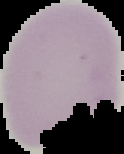 Result: no malaria parasites detected. Cell region segmented out of the field of view; the surrounding area is masked to black. Image is 124×154 pixels. From a thin blood film.